Draw a bounding box around every malaria parasite.
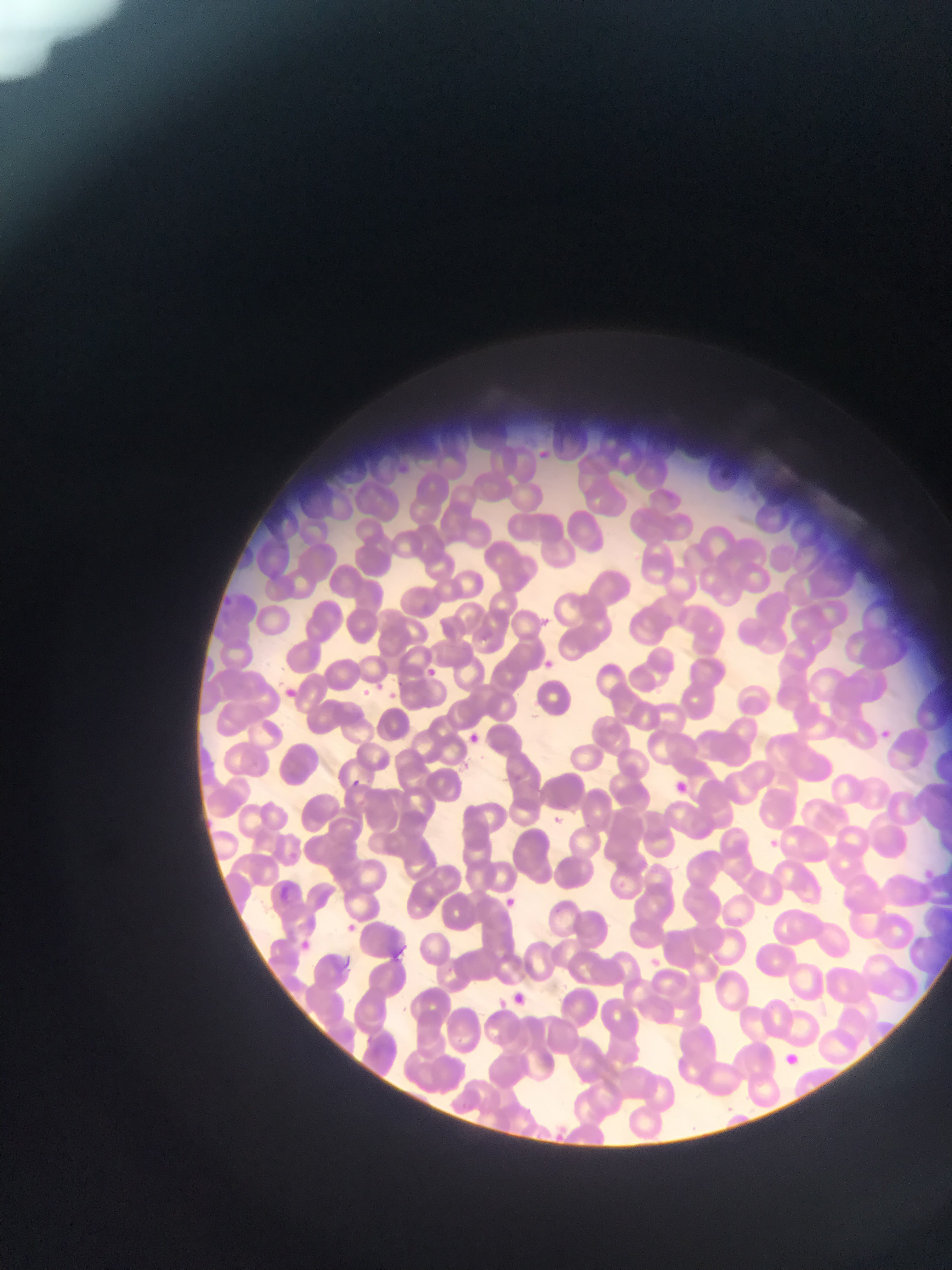
Approximate bounding boxes as left top right bottom in pixels.
Malaria parasites: 537 614 555 628; 540 658 554 670; 429 667 441 681; 375 679 388 689; 358 686 368 699; 385 687 402 699; 875 727 891 740; 464 732 482 740; 351 776 368 788; 766 835 784 849; 276 882 297 901; 502 897 519 911; 344 919 362 929.

field of view = single
capture = mobile-phone photograph through a microscope
preparation = thin blood smear
image size = 952×1270 pixels
country = Ghana